Assess the morphology of the erythrocytes.
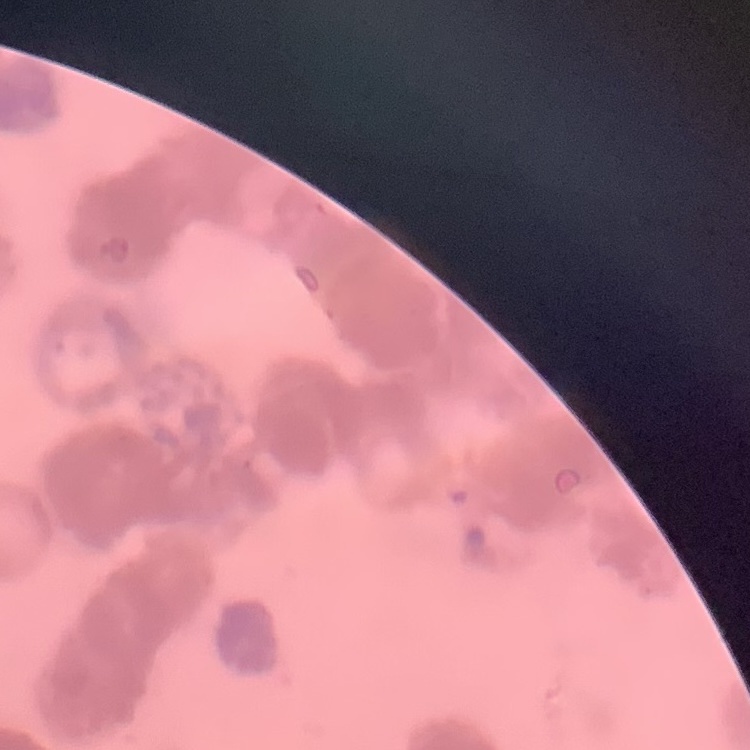
They show rouleaux formation.

Summary:
  - Stain: Field's or Giemsa
  - Image type: one tile cut from a larger photomicrograph
  - Preparation: thin blood film